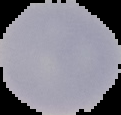
Summary:
  - Image size: 121×115 pixels
  - Result: no Plasmodium parasites detected
  - Image type: segmented cell region on a black background
  - Preparation: thin blood film